Locate every blood parasite and identify its species.
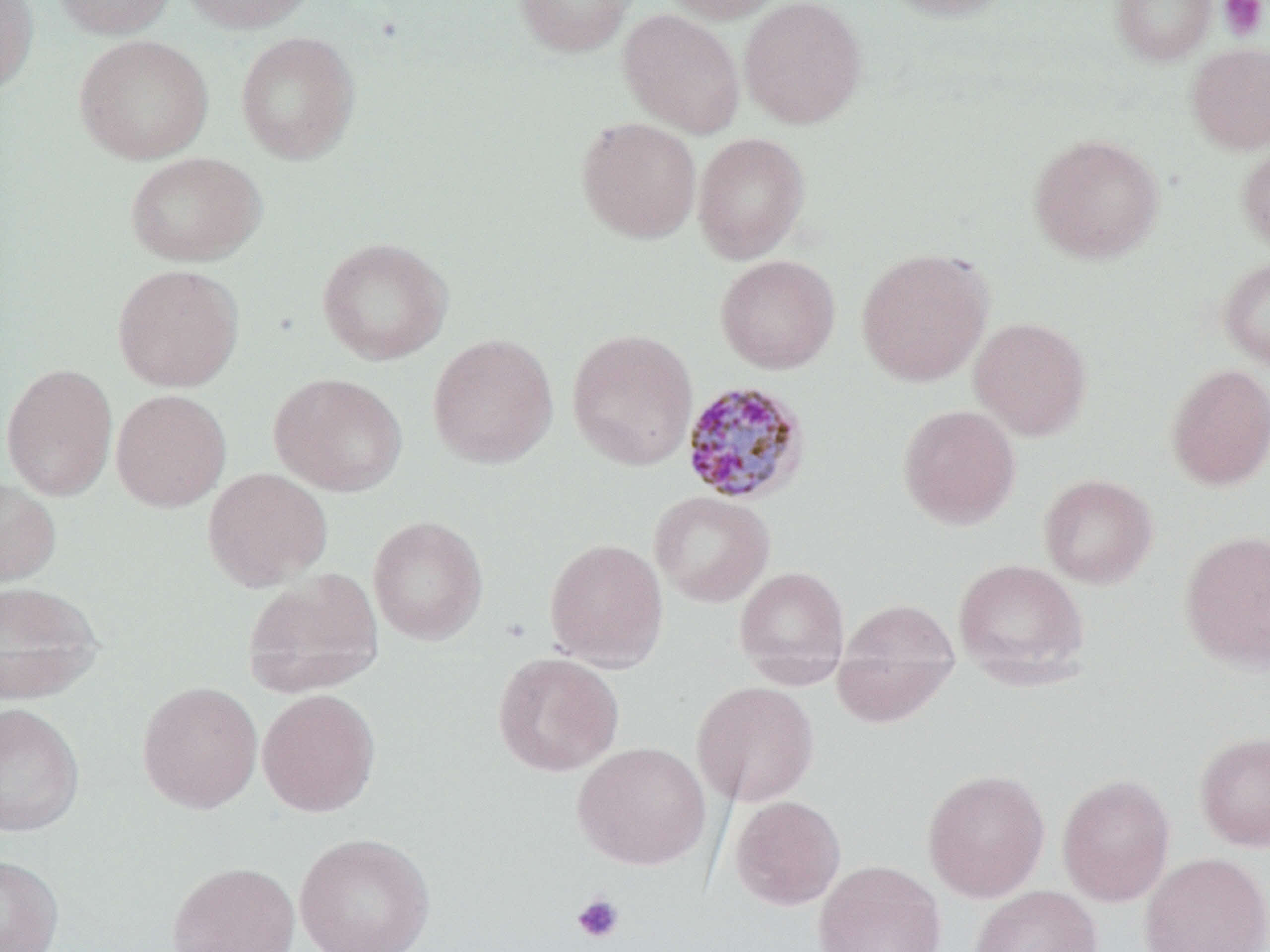
Approximate bounding boxes as (x1, y1, x2, y2) in pixels.
Plasmodium malariae-infected red blood cells: (680, 380, 810, 505).
No Plasmodium falciparum, Plasmodium ovale, Plasmodium vivax, Babesia divergens, or Trypanosoma brucei observed.

slide-level diagnosis = Plasmodium malariae
stain = May-Grünwald-Giemsa
magnification = 1000x
preparation = thin blood film
platelet locations = approximate bounding boxes as (x1, y1, x2, y2) in pixels: (1218, 0, 1268, 41), (571, 893, 625, 944)
modality = light microscopy
image size = 1270×952 pixels
uninfected red blood cell locations = approximate bounding boxes as (x1, y1, x2, y2) in pixels: (0, 0, 39, 95), (51, 0, 176, 39), (178, 0, 316, 34), (514, 0, 638, 57), (660, 0, 786, 24), (739, 0, 867, 129), (881, 0, 1017, 21), (1111, 0, 1217, 65), (618, 9, 745, 138), (236, 31, 360, 164), (74, 34, 213, 164), (1185, 43, 1270, 154), (576, 117, 701, 243), (692, 132, 810, 263), (1027, 134, 1165, 264), (1237, 142, 1270, 254), (125, 151, 266, 267), (317, 237, 452, 365), (856, 248, 993, 386), (715, 254, 840, 374), (1218, 257, 1270, 371), (112, 264, 244, 392), (969, 316, 1092, 440), (566, 329, 699, 470), (427, 333, 558, 469), (1, 363, 118, 500), (1165, 363, 1270, 491), (269, 373, 408, 496), (111, 389, 231, 511), (897, 404, 1020, 529), (202, 466, 334, 591), (1038, 474, 1158, 588), (0, 475, 61, 588), (649, 491, 775, 607), (367, 515, 488, 645), (1179, 531, 1270, 672), (544, 538, 668, 671), (952, 559, 1089, 682), (733, 565, 850, 684), (241, 569, 384, 696), (0, 580, 103, 703), (834, 597, 960, 713), (492, 652, 624, 777), (137, 681, 263, 813), (692, 681, 819, 807), (257, 688, 381, 817), (0, 702, 85, 837), (1194, 731, 1270, 851), (572, 741, 711, 870), (922, 768, 1050, 902), (1057, 773, 1175, 906), (730, 795, 846, 910), (294, 832, 436, 952), (1139, 851, 1270, 952), (0, 854, 64, 952), (813, 859, 946, 952), (166, 861, 300, 952), (969, 885, 1103, 952)
field of view = one of a larger specimen